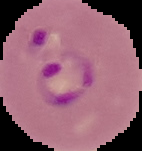

Image is 142×151 pixels. From a thin blood film. Cell region segmented out of the field of view; the surrounding area is masked to black. Result: malaria parasites identified.